Classify this cell by malaria status.
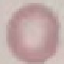
Uninfected.

stain = Giemsa
preparation = thin smear
capture = smartphone through the microscope eyepiece
image type = automatically extracted cell patch, resized to 64 × 64 pixels